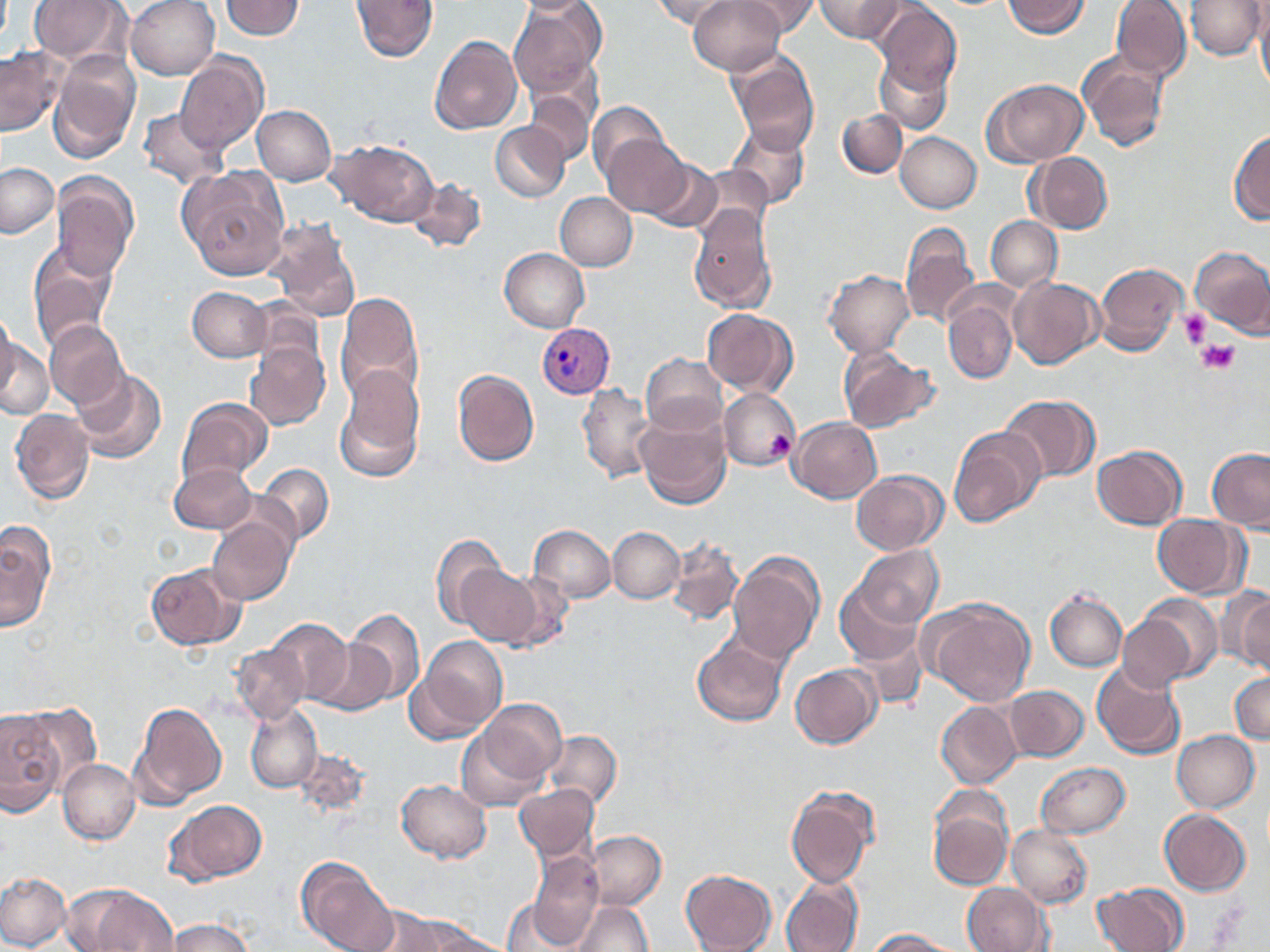
Summary:
  - Coordinate format: approximate bounding boxes as [x1, y1, x2, y2] in pixels
  - Uninfected red blood cell locations: [26, 0, 130, 65], [126, 0, 219, 79], [219, 0, 306, 40], [350, 0, 438, 62], [650, 0, 735, 29], [688, 0, 788, 73], [737, 0, 820, 35], [813, 0, 910, 43], [1002, 0, 1091, 37], [1109, 0, 1192, 81], [1186, 0, 1264, 60], [508, 2, 606, 100], [873, 5, 961, 100], [1256, 5, 1270, 94], [429, 35, 523, 135], [0, 44, 68, 138], [726, 49, 820, 156], [1076, 50, 1170, 156], [48, 52, 140, 164], [175, 52, 268, 156], [876, 54, 953, 134], [984, 78, 1089, 166], [522, 80, 597, 167], [587, 100, 675, 189], [140, 106, 228, 193], [252, 106, 336, 185], [837, 109, 908, 179], [490, 121, 570, 203], [726, 124, 812, 213], [598, 129, 692, 217], [1228, 129, 1270, 226], [896, 132, 981, 213], [328, 138, 437, 226], [1029, 152, 1113, 233], [630, 153, 724, 233], [1, 163, 58, 239], [177, 164, 291, 279], [52, 176, 137, 282], [408, 177, 486, 253], [555, 192, 638, 270], [688, 204, 779, 313], [986, 215, 1062, 292], [265, 217, 360, 321], [901, 222, 979, 329], [26, 243, 119, 350], [1191, 246, 1270, 339], [499, 249, 590, 332], [1094, 261, 1187, 357], [823, 270, 915, 356], [1009, 277, 1102, 369], [187, 285, 271, 362], [334, 292, 425, 407], [943, 298, 1016, 384], [703, 308, 797, 396], [0, 318, 49, 423], [45, 321, 128, 409], [246, 343, 330, 430], [836, 347, 940, 435], [641, 352, 728, 436], [332, 363, 426, 484], [69, 366, 167, 464], [453, 368, 540, 466], [577, 384, 657, 483], [719, 386, 800, 470], [997, 394, 1100, 485], [177, 397, 272, 484], [10, 408, 94, 505], [634, 410, 731, 510], [789, 416, 883, 502], [949, 426, 1046, 529], [1092, 444, 1188, 529], [1208, 447, 1270, 531], [169, 464, 258, 531], [256, 464, 335, 547], [176, 467, 275, 583], [851, 470, 946, 555], [207, 513, 296, 605], [1153, 514, 1245, 598], [529, 524, 615, 604], [0, 525, 52, 631], [609, 526, 683, 604], [430, 532, 512, 629], [667, 538, 744, 624], [853, 543, 944, 630], [729, 551, 825, 667], [142, 561, 246, 650], [458, 562, 548, 649], [491, 569, 575, 653], [836, 576, 926, 665], [1044, 588, 1128, 673], [1224, 589, 1270, 674], [923, 599, 1036, 706], [1117, 600, 1214, 692], [346, 606, 425, 706], [265, 617, 354, 708], [413, 635, 507, 740], [692, 636, 787, 726], [308, 640, 397, 717], [233, 642, 310, 723], [1092, 661, 1184, 761], [790, 664, 880, 747], [1230, 669, 1270, 745], [1005, 684, 1088, 762], [465, 695, 569, 800], [128, 699, 227, 808], [12, 701, 99, 794], [936, 702, 1021, 788], [247, 704, 322, 793], [0, 709, 62, 819], [544, 730, 622, 813], [1172, 730, 1260, 812], [58, 757, 141, 845], [1024, 760, 1125, 917], [1036, 761, 1131, 838], [395, 778, 492, 863], [514, 783, 600, 865], [784, 787, 878, 887], [928, 789, 1015, 889], [164, 797, 268, 885], [1158, 808, 1251, 895], [1007, 825, 1092, 907], [585, 829, 667, 909], [525, 849, 604, 950], [296, 856, 399, 951], [680, 868, 778, 952], [0, 870, 71, 951], [780, 875, 863, 952], [1093, 881, 1187, 952], [963, 883, 1052, 952], [88, 887, 180, 952], [569, 899, 653, 952], [366, 910, 476, 951], [163, 916, 257, 951], [864, 928, 961, 951]
  - Plasmodium vivax-infected red blood cell locations: [537, 322, 614, 397]
  - Platelet locations: [1176, 308, 1212, 346], [1183, 326, 1231, 373], [1200, 339, 1237, 373], [766, 431, 795, 460]
  - Slide-level diagnosis: Plasmodium vivax
  - Field of view: one of a larger specimen
  - Image size: 1270×952 pixels
  - Stain: May-Grünwald-Giemsa
  - Preparation: thin blood smear
  - Magnification: 1000x
  - Modality: optical microscopy